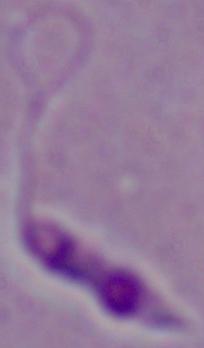

Summary:
  - Magnification: 1000x
  - Identification: Leishmania
  - Modality: photomicrograph